Name the parasite shown.
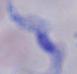
This is a trypanosome.

{
  "modality": "photomicrograph",
  "magnification": "1000x"
}